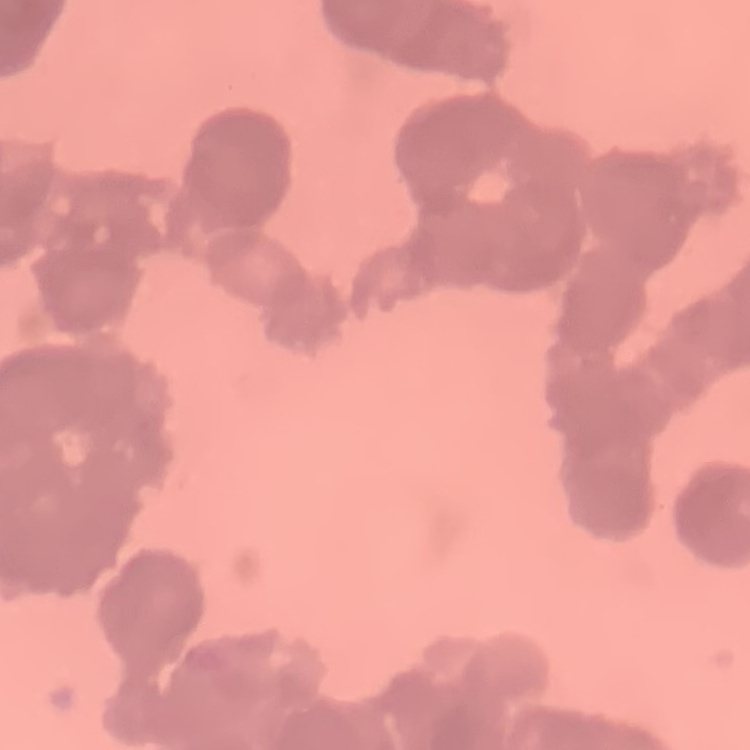

{
  "red_blood_cell_morphology": "rouleaux formation",
  "preparation": "thin blood smear",
  "stain": "Field's or Giemsa",
  "image_type": "one tile cut from a larger photomicrograph"
}